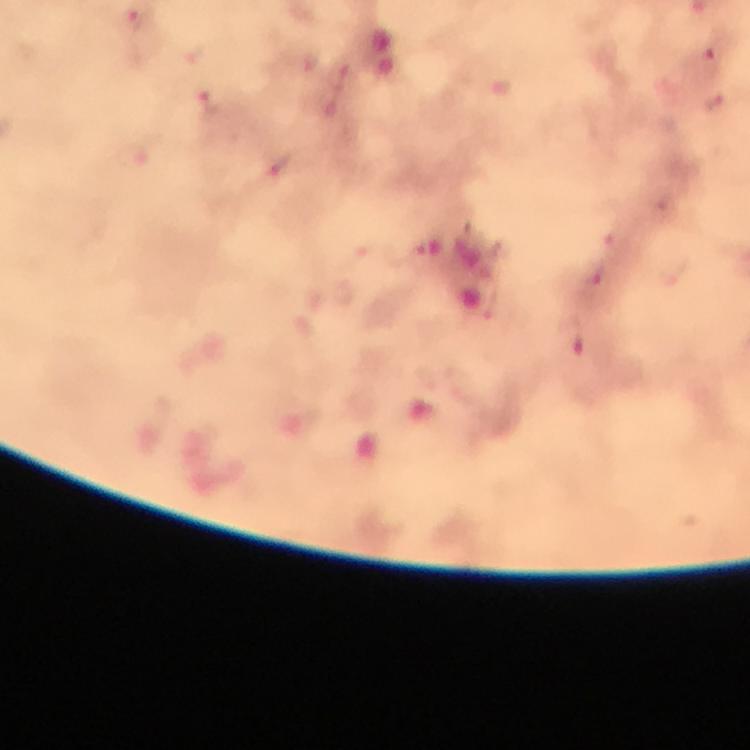

Approximate centers as (x, y) in pixels. Malaria parasite locations: (708, 61), (715, 102), (597, 276), (574, 338). Image is 750×750 pixels. Thick blood film. At 100x magnification. From a malaria diagnostic workup. Photographed through the microscope with a smartphone camera. Immersion oil was used. Giemsa stain. Cropped region of a single field of view.